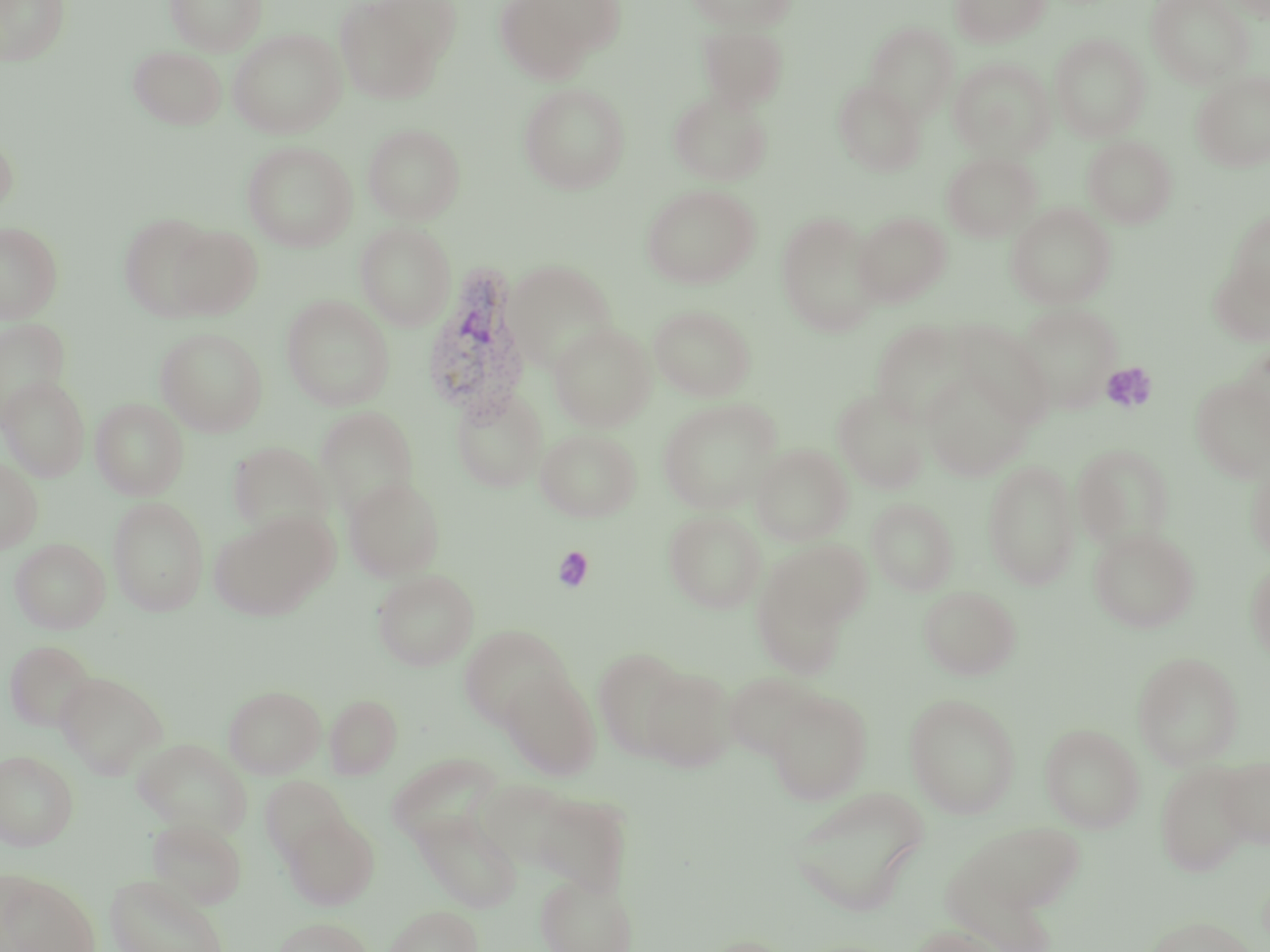 Approximate bounding boxes as (x1, y1, x2, y2) in pixels. Plasmodium vivax-infected red blood cell locations: (421, 267, 532, 424). Uninfected red blood cell locations: (0, 0, 71, 67), (165, 0, 266, 55), (334, 0, 455, 104), (495, 0, 605, 84), (525, 0, 629, 58), (686, 0, 797, 32), (949, 0, 1051, 48), (1146, 0, 1255, 87), (865, 22, 958, 121), (697, 24, 789, 112), (228, 28, 346, 138), (1050, 34, 1150, 141), (128, 45, 227, 129), (948, 58, 1055, 161), (1192, 70, 1270, 172), (832, 80, 926, 176), (519, 82, 630, 194), (668, 91, 773, 186), (363, 123, 465, 224), (0, 130, 19, 221), (1082, 135, 1178, 228), (242, 141, 358, 251), (942, 151, 1041, 242), (641, 184, 760, 289), (1006, 203, 1116, 308), (1228, 211, 1269, 308), (776, 212, 883, 336), (852, 212, 952, 307), (119, 214, 217, 319), (0, 221, 63, 323), (355, 221, 456, 330), (167, 225, 263, 319), (1208, 256, 1270, 347), (503, 260, 618, 372), (281, 294, 395, 410), (1012, 302, 1122, 413), (649, 305, 756, 401), (0, 318, 71, 426), (871, 319, 973, 426), (955, 321, 1054, 427), (549, 323, 656, 432), (156, 327, 267, 436), (1236, 342, 1270, 440), (922, 370, 1032, 480), (1, 375, 89, 480), (1189, 376, 1270, 482), (451, 386, 548, 493), (833, 387, 930, 494), (90, 398, 189, 500), (658, 398, 783, 514), (315, 406, 419, 518), (535, 428, 642, 522), (228, 440, 334, 539), (1072, 442, 1176, 550), (751, 444, 853, 546), (1245, 448, 1270, 564), (0, 457, 43, 553), (983, 459, 1081, 590), (343, 476, 446, 582), (108, 497, 209, 616), (866, 498, 958, 595), (664, 509, 766, 614), (210, 512, 336, 621), (1088, 526, 1200, 633), (10, 538, 110, 634), (761, 539, 872, 636), (1245, 558, 1270, 667), (372, 569, 479, 670), (752, 572, 852, 680), (919, 585, 1021, 680), (458, 624, 572, 729), (5, 640, 97, 732), (593, 647, 690, 761), (1132, 651, 1244, 769), (640, 666, 737, 773), (499, 669, 601, 780), (55, 671, 167, 778), (722, 671, 824, 760), (223, 685, 326, 778), (766, 689, 872, 804), (325, 693, 402, 779), (904, 693, 1021, 818), (1039, 723, 1145, 833), (133, 737, 250, 837), (0, 750, 78, 850), (386, 752, 504, 848), (1217, 756, 1270, 849), (1155, 760, 1256, 876), (260, 776, 350, 863), (473, 777, 584, 871), (789, 786, 930, 916), (529, 790, 633, 897), (412, 810, 523, 912), (282, 814, 379, 909), (147, 817, 247, 909), (951, 820, 1084, 931), (0, 870, 100, 952), (104, 873, 230, 952), (535, 874, 637, 952), (384, 904, 482, 952), (1145, 915, 1259, 952), (272, 917, 374, 952), (910, 925, 1010, 952), (694, 936, 799, 952). Platelet locations: (1101, 362, 1158, 414), (552, 546, 594, 592). Slide-level diagnosis: Plasmodium vivax. May-Grünwald-Giemsa stain. Image is 1270×952 pixels. 1000x magnification. One field of a larger specimen. Thin blood smear. Optical microscopy.